Classify this cell by malaria status.
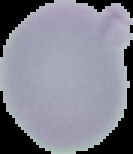
It is uninfected.

Summary:
  - Image type: cell region segmented out of the field of view; surrounding area masked to black
  - Preparation: thin blood film
  - Image size: 133×154 pixels